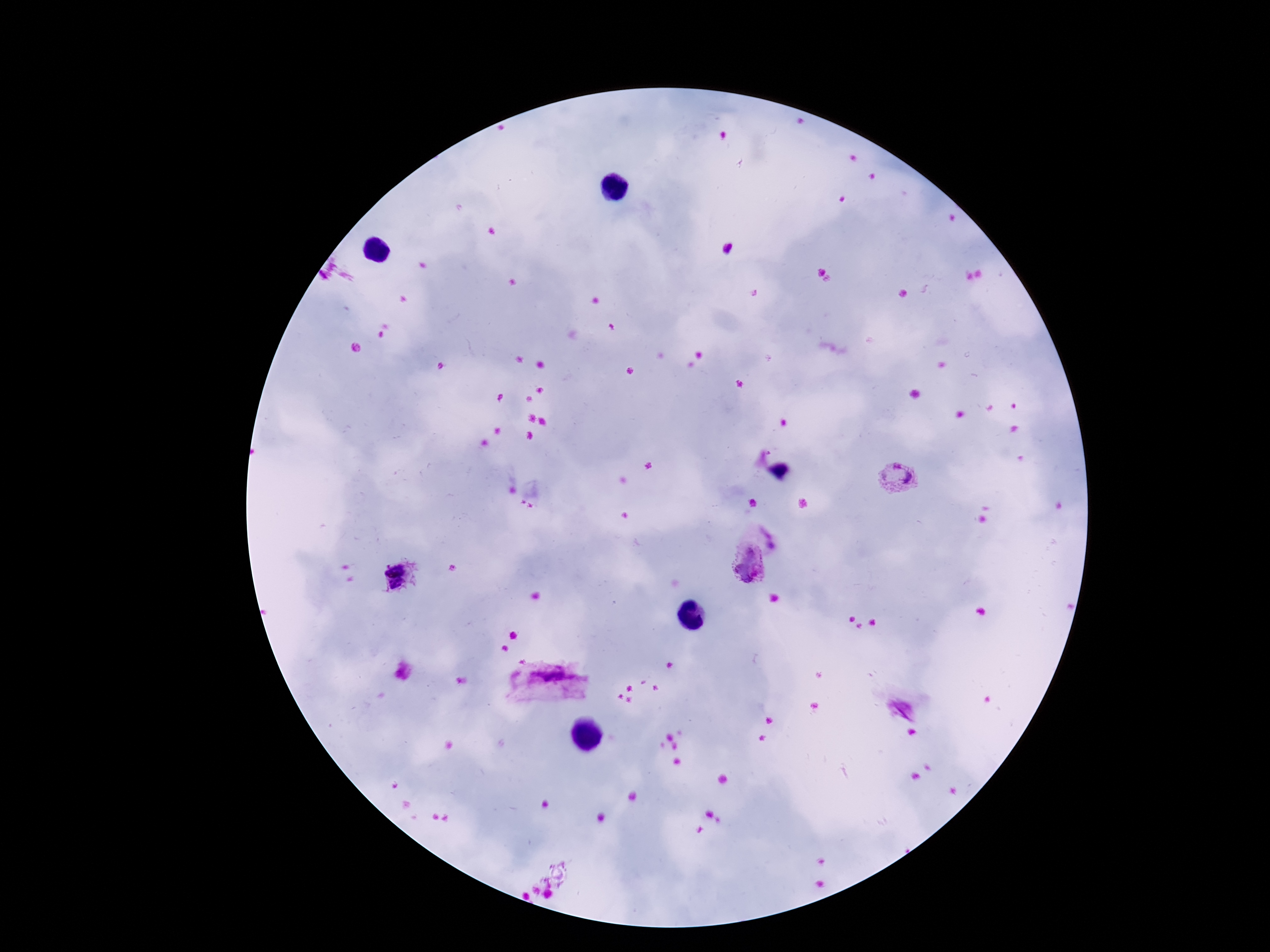 Approximate object centers, in pixels from the top-left corner. Plasmodium parasite locations: (x=896, y=477), (x=748, y=564), (x=549, y=683), (x=900, y=710). One field from this slide. Thick peripheral-blood smear. Giemsa-stained preparation. Smartphone photograph taken through the microscope eyepiece. Image is 1270×952 pixels. 100x magnification. Patient malaria status: positive.